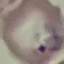
malaria_status: parasitized
capture: smartphone camera at the microscope eyepiece
stain: Giemsa
preparation: thin blood film
image_type: cell patch, automatically extracted from a larger field of view and resized to 64 × 64 pixels